Identify the parasite.
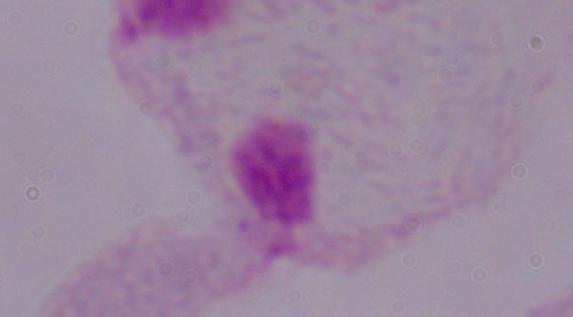

A trichomonad.

magnification = 1000x
modality = photomicrograph